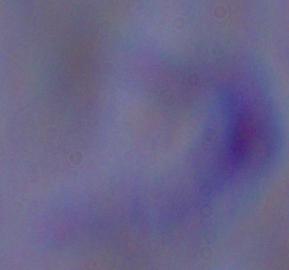
modality = photomicrograph
magnification = 1000x
identification = trypanosome